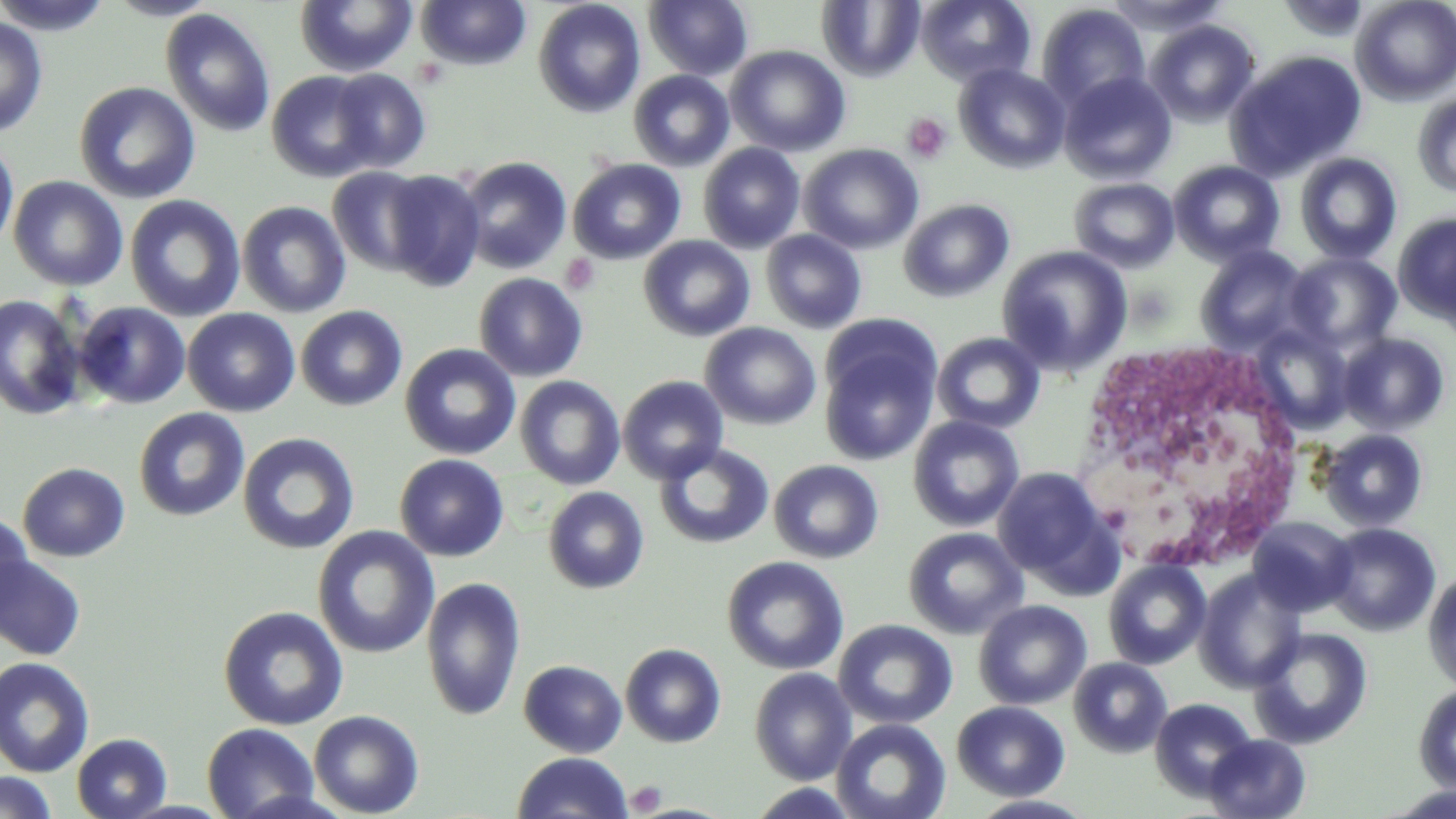
Summary:
  - Coordinate format: approximate bounding boxes as (x1, y1, x2, y2) in pixels
  - Platelet locations: (903, 113, 952, 163), (560, 254, 601, 294), (626, 781, 667, 815)
  - White blood cell locations: (1078, 339, 1303, 558)
  - Uninfected red blood cell locations: (0, 0, 114, 35), (104, 0, 222, 21), (294, 0, 417, 77), (643, 0, 753, 81), (915, 0, 1036, 86), (1104, 0, 1230, 36), (1278, 0, 1372, 42), (1351, 0, 1456, 105), (415, 1, 531, 70), (532, 1, 646, 118), (817, 1, 925, 82), (1037, 3, 1150, 110), (160, 8, 276, 138), (0, 14, 48, 138), (1145, 19, 1261, 127), (725, 45, 850, 157), (1226, 49, 1367, 180), (953, 63, 1070, 174), (329, 68, 431, 174), (628, 69, 735, 171), (266, 70, 381, 183), (1059, 71, 1176, 184), (74, 81, 201, 204), (1412, 91, 1456, 198), (0, 137, 19, 254), (698, 143, 805, 253), (798, 144, 924, 254), (1294, 152, 1402, 264), (458, 156, 573, 274), (567, 158, 686, 265), (1168, 160, 1285, 266), (328, 166, 433, 276), (380, 169, 485, 292), (8, 175, 128, 291), (1069, 178, 1179, 272), (125, 194, 246, 322), (899, 198, 1014, 302), (237, 200, 351, 317), (1394, 212, 1456, 325), (760, 229, 867, 334), (639, 236, 755, 341), (996, 245, 1132, 376), (1194, 245, 1312, 353), (1285, 252, 1401, 354), (474, 272, 589, 382), (0, 294, 86, 421), (73, 302, 190, 408), (295, 305, 408, 411), (183, 308, 300, 416), (700, 322, 821, 430), (1246, 324, 1354, 435), (819, 328, 942, 466), (931, 332, 1045, 434), (1338, 333, 1450, 436), (399, 343, 521, 460), (514, 376, 625, 490), (617, 376, 729, 484), (133, 408, 249, 521), (907, 415, 1025, 532), (1318, 429, 1428, 533), (237, 432, 360, 555), (654, 443, 774, 549), (394, 454, 509, 561), (768, 459, 884, 564), (17, 462, 130, 562), (991, 466, 1114, 587), (542, 486, 650, 594), (0, 511, 34, 627), (1248, 517, 1356, 616), (1323, 522, 1442, 636), (313, 526, 439, 659), (903, 526, 1028, 640), (0, 554, 87, 661), (721, 556, 848, 675), (1102, 559, 1211, 670), (1194, 570, 1307, 692), (1422, 570, 1456, 692), (421, 577, 526, 722), (974, 600, 1092, 710), (218, 605, 348, 730), (834, 619, 957, 729), (1250, 627, 1372, 749), (619, 642, 726, 748), (0, 657, 95, 777), (1068, 657, 1172, 758), (518, 660, 627, 757), (749, 667, 857, 785), (1413, 684, 1456, 794), (1149, 697, 1257, 802), (952, 700, 1070, 801), (308, 710, 425, 817), (831, 718, 951, 819), (201, 722, 320, 819), (72, 733, 172, 818), (1204, 734, 1311, 818), (511, 752, 633, 818), (0, 771, 58, 819), (745, 783, 861, 818), (1380, 784, 1456, 818), (967, 794, 1097, 818)
  - Slide-level diagnosis: negative for blood parasites
  - Stain: May-Grünwald-Giemsa
  - Image size: 1456×819 pixels
  - Magnification: 1000x
  - Preparation: thin blood smear
  - Modality: light microscopy
  - Field of view: one of a larger specimen